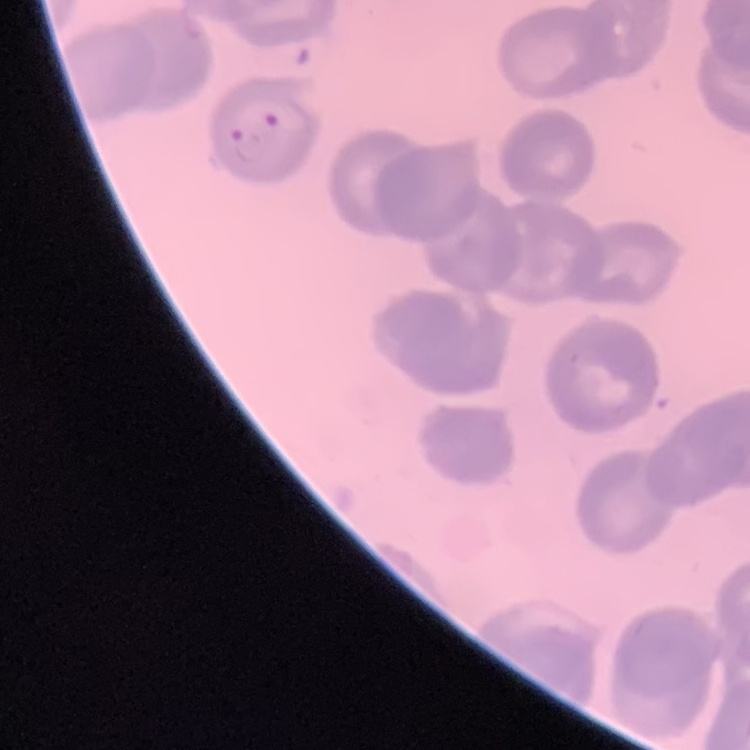

{
  "red_blood_cell_morphology": "no rouleaux formation",
  "image_type": "one tile cut from a larger photomicrograph",
  "stain": "Field's or Giemsa",
  "preparation": "thin peripheral smear"
}